Locate every blood parasite and identify its species.
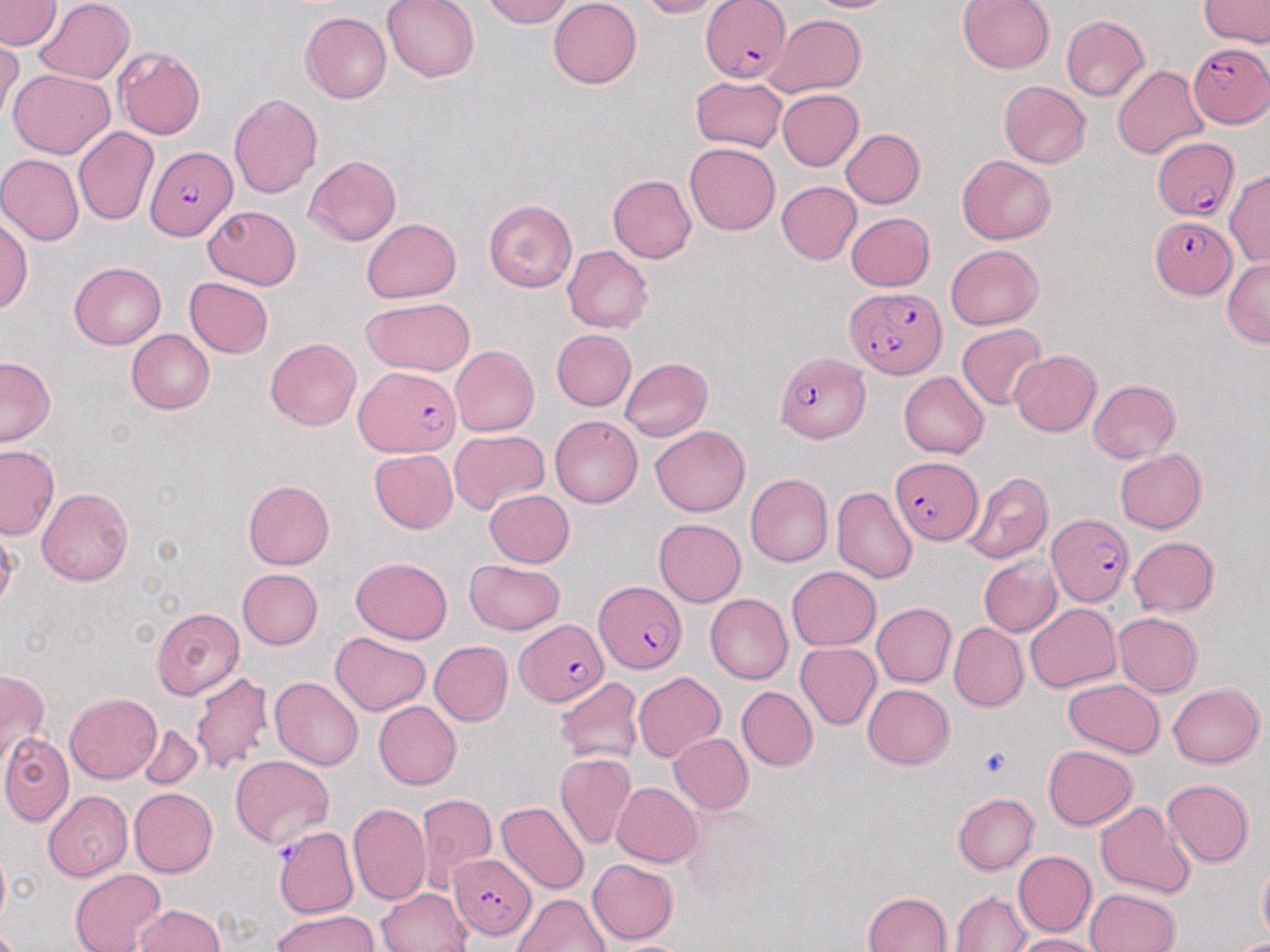
Approximate bounding boxes as (x1, y1, x2, y2) in pixels.
Plasmodium falciparum-infected red blood cells: (701, 1, 791, 84), (1188, 43, 1269, 126), (1151, 140, 1238, 223), (146, 146, 237, 240), (1151, 217, 1235, 300), (846, 288, 946, 379), (774, 352, 869, 443), (356, 367, 462, 456), (891, 456, 984, 545), (1048, 513, 1135, 606), (595, 582, 685, 673), (519, 620, 607, 705), (449, 854, 538, 940).
No Plasmodium ovale, Plasmodium malariae, Plasmodium vivax, Babesia divergens, or Trypanosoma brucei observed.

Summary:
  - Platelet locations: (978, 746, 1014, 781)
  - Uninfected red blood cell locations: (0, 0, 61, 50), (35, 0, 135, 85), (381, 0, 480, 83), (482, 0, 572, 27), (547, 0, 642, 89), (636, 0, 719, 19), (803, 0, 900, 12), (956, 0, 1055, 74), (1200, 0, 1269, 48), (300, 13, 391, 104), (765, 14, 866, 97), (1060, 15, 1150, 101), (1, 38, 23, 127), (113, 47, 205, 139), (1113, 65, 1208, 159), (8, 69, 114, 159), (691, 75, 786, 152), (997, 80, 1091, 168), (777, 89, 864, 170), (228, 94, 323, 199), (73, 127, 159, 227), (840, 128, 925, 209), (686, 142, 780, 234), (0, 154, 84, 246), (305, 155, 401, 247), (956, 156, 1055, 244), (1225, 168, 1270, 266), (607, 174, 697, 263), (776, 181, 862, 264), (483, 198, 577, 292), (203, 205, 301, 290), (846, 212, 935, 290), (361, 217, 461, 303), (0, 219, 32, 312), (944, 244, 1045, 330), (562, 246, 652, 334), (1221, 257, 1270, 348), (69, 261, 166, 350), (184, 278, 272, 359), (361, 298, 475, 376), (956, 323, 1046, 409), (126, 329, 214, 414), (551, 329, 635, 412), (265, 337, 361, 431), (451, 346, 539, 437), (1009, 350, 1101, 437), (0, 357, 56, 446), (620, 357, 712, 440), (899, 371, 989, 458), (1088, 379, 1180, 462), (550, 415, 643, 508), (650, 425, 750, 516), (449, 430, 549, 515), (0, 445, 59, 540), (370, 449, 458, 532), (1115, 449, 1207, 533), (961, 471, 1053, 565), (746, 474, 833, 567), (243, 479, 334, 569), (37, 487, 133, 586), (831, 487, 918, 584), (484, 489, 574, 568), (653, 518, 746, 607), (1127, 536, 1219, 617), (978, 555, 1063, 637), (350, 556, 452, 643), (465, 559, 566, 635), (786, 565, 881, 651), (237, 568, 323, 648), (705, 592, 792, 685), (871, 603, 956, 687), (1026, 603, 1122, 691), (151, 608, 245, 699), (1112, 613, 1204, 696), (949, 622, 1028, 712), (329, 632, 431, 715), (429, 641, 512, 726), (795, 642, 880, 730), (1, 668, 49, 768), (189, 671, 274, 775), (633, 672, 725, 762), (555, 677, 643, 767), (269, 678, 363, 770), (1063, 680, 1165, 758), (1167, 683, 1265, 768), (863, 684, 954, 770), (736, 686, 818, 771), (66, 692, 162, 784), (372, 701, 461, 790), (138, 725, 203, 788), (1, 733, 74, 826), (668, 733, 753, 813), (1043, 745, 1138, 830), (555, 752, 637, 850), (230, 755, 334, 848), (1162, 779, 1255, 866), (612, 781, 702, 867), (130, 787, 218, 877), (44, 792, 133, 881), (953, 792, 1038, 875), (416, 793, 497, 882), (498, 800, 590, 894), (348, 802, 430, 904), (679, 802, 779, 905), (1096, 802, 1197, 900), (279, 831, 358, 921), (0, 844, 10, 931), (1012, 850, 1096, 938), (587, 858, 678, 944), (1257, 859, 1270, 947), (69, 869, 166, 951), (376, 888, 472, 952), (1086, 888, 1180, 952), (949, 890, 1033, 951), (863, 891, 952, 952), (513, 893, 610, 952), (135, 904, 227, 951), (272, 910, 381, 952), (1013, 934, 1103, 952), (605, 940, 694, 952)
  - Slide-level diagnosis: Plasmodium falciparum
  - Magnification: 1000x
  - Modality: light microscopy
  - Preparation: thin blood film
  - Image size: 1270×952 pixels
  - Stain: May-Grünwald-Giemsa
  - Field of view: one of a larger specimen